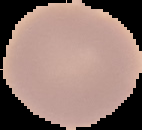

{
  "preparation": "thin blood smear",
  "image_type": "segmented cell region on a black background",
  "image_size": "142×130 pixels",
  "malaria_status": "uninfected"
}